Locate every blood parasite and identify its species.
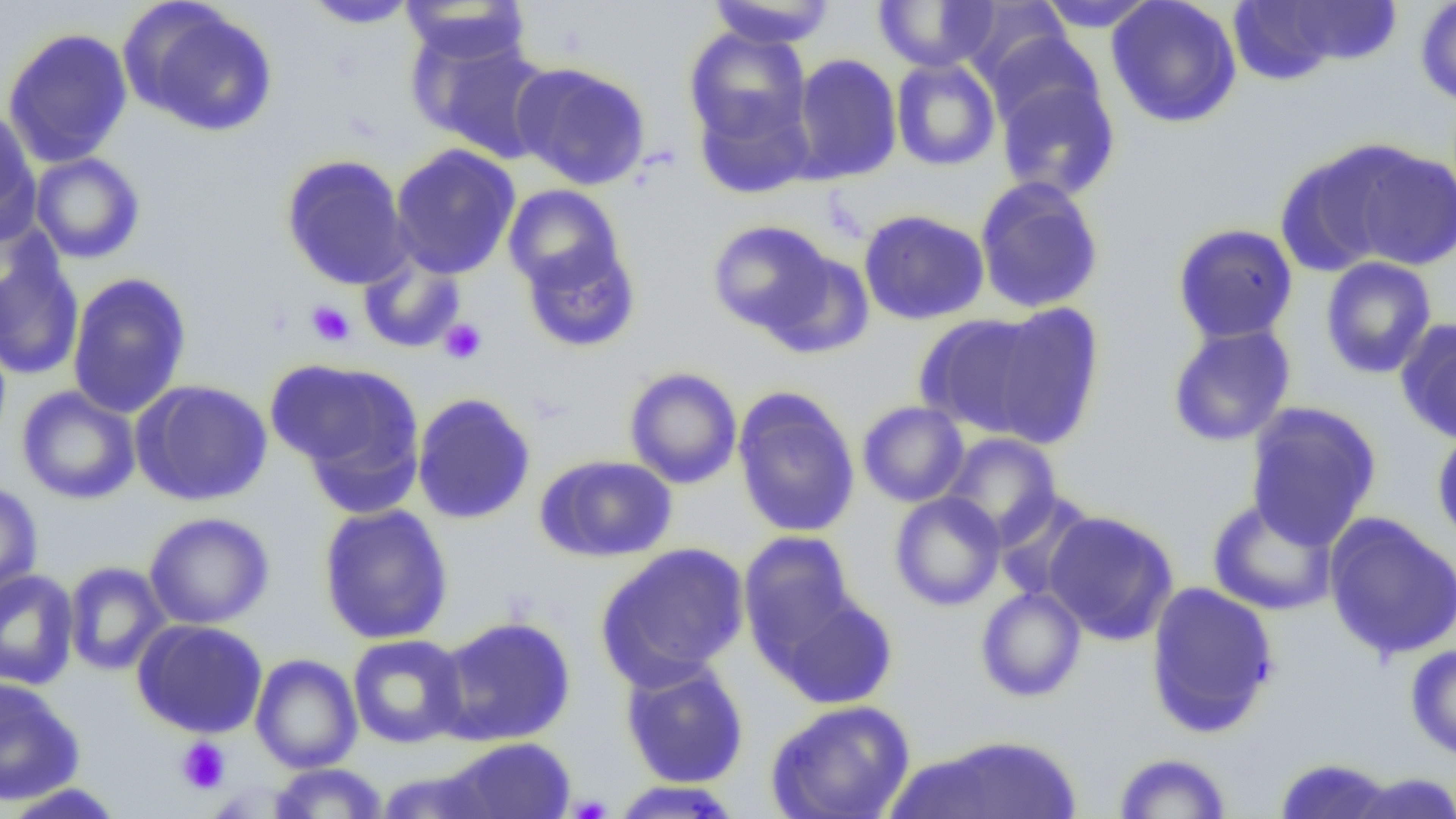
No blood parasites observed.

slide-level diagnosis = negative for blood parasites
field of view = single
uninfected red blood cell locations = approximate bounding boxes as (x1, y1, x2, y2) in pixels: (399, 0, 532, 64), (705, 0, 838, 49), (1034, 0, 1160, 33), (1105, 0, 1242, 128), (1415, 0, 1456, 107), (303, 1, 421, 29), (871, 1, 1000, 72), (124, 2, 277, 136), (957, 2, 1072, 87), (1235, 2, 1403, 79), (2, 27, 133, 167), (684, 27, 812, 148), (409, 29, 555, 163), (983, 31, 1104, 135), (790, 53, 903, 184), (890, 58, 1001, 171), (512, 61, 651, 190), (995, 75, 1120, 201), (693, 89, 814, 199), (0, 107, 40, 242), (390, 143, 521, 279), (1342, 144, 1456, 272), (1275, 147, 1404, 277), (30, 152, 145, 264), (281, 154, 412, 290), (974, 176, 1105, 314), (503, 184, 623, 292), (859, 209, 989, 325), (706, 219, 834, 334), (1172, 223, 1299, 345), (521, 241, 641, 353), (0, 246, 84, 382), (762, 250, 875, 359), (358, 252, 466, 354), (1319, 257, 1437, 379), (66, 272, 192, 419), (982, 302, 1105, 449), (916, 314, 1050, 437), (1396, 319, 1456, 444), (1167, 324, 1296, 447), (267, 358, 424, 501), (624, 367, 742, 489), (132, 379, 273, 506), (15, 385, 141, 505), (733, 389, 860, 538), (411, 392, 537, 525), (857, 401, 970, 507), (1244, 401, 1382, 549), (1431, 426, 1456, 551), (940, 433, 1062, 545), (537, 455, 677, 562), (0, 481, 43, 600), (889, 491, 1006, 611), (1206, 498, 1339, 616), (318, 504, 454, 645), (1043, 510, 1179, 645), (144, 511, 274, 630), (1323, 512, 1456, 661), (738, 530, 857, 661), (596, 542, 749, 687), (63, 561, 172, 675), (0, 568, 79, 690), (1145, 581, 1280, 737), (975, 586, 1087, 702), (776, 594, 898, 709), (434, 615, 577, 746), (132, 618, 268, 738), (347, 634, 468, 748), (1405, 644, 1456, 761), (250, 653, 362, 773), (620, 660, 749, 788), (0, 678, 84, 806), (764, 699, 916, 819), (898, 734, 1084, 819), (440, 737, 577, 819), (1112, 752, 1234, 818), (1273, 757, 1398, 818), (268, 763, 389, 818), (1343, 772, 1456, 818), (609, 780, 743, 818), (2, 783, 126, 818)
modality = optical microscopy
preparation = thin blood film
magnification = 1000x
platelet locations = approximate bounding boxes as (x1, y1, x2, y2) in pixels: (305, 300, 355, 347), (439, 318, 488, 364), (175, 737, 230, 794)
image size = 1456×819 pixels